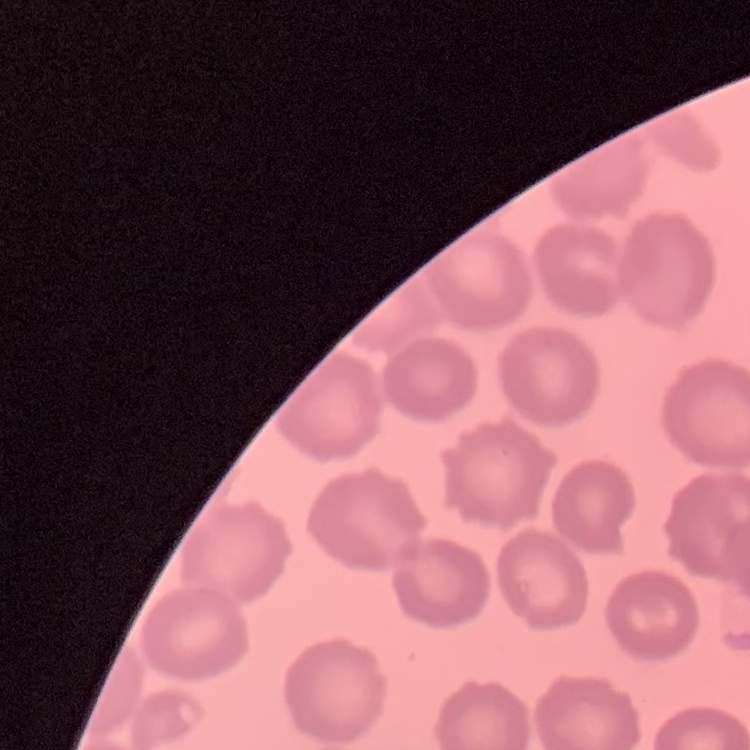
The red blood cells show no rouleaux formation. Square crop of a larger photomicrograph. Field's or Giemsa stain. Thin blood film.